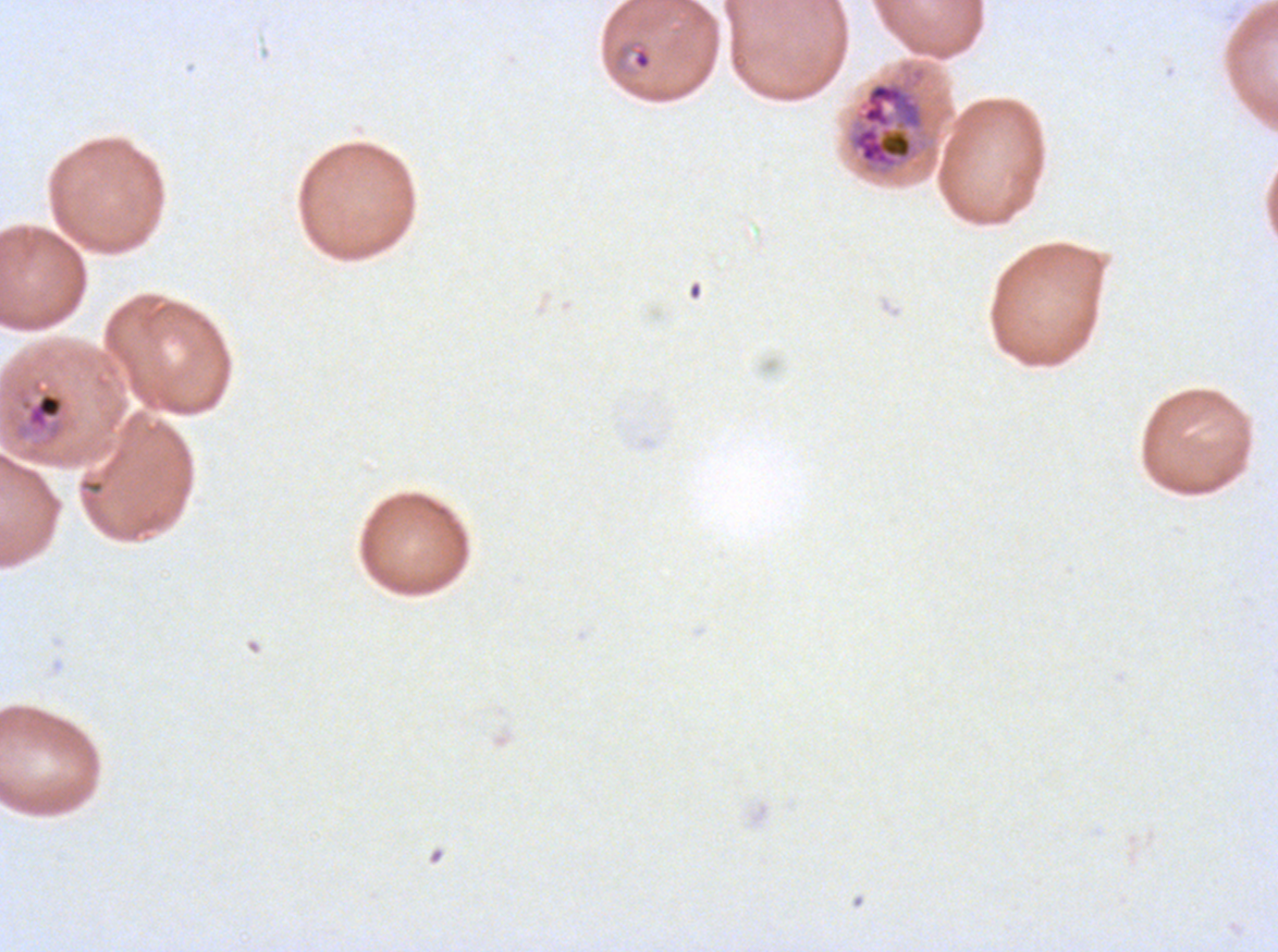
Approximate bounding boxes as {x1, y1, x2, y2} in pixels. Ring locations: {615, 39, 653, 71}, {20, 391, 65, 432}. Late trophozoite locations: {848, 81, 926, 172}. Giemsa-stained preparation. Ex-vivo Plasmodium falciparum culture from a patient in The Gambia, grown for 24 to 48 hours. Thin blood film. Image is 1278×952 pixels. One sub-image of a larger composite. Life-cycle stages observed: ring, late trophozoite.